Assess this cell for malaria.
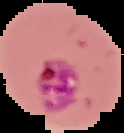
It is parasitized.

image size = 124×133 pixels
image type = segmented cell region with the area outside set to black
preparation = thin blood smear